Give the preparation type.
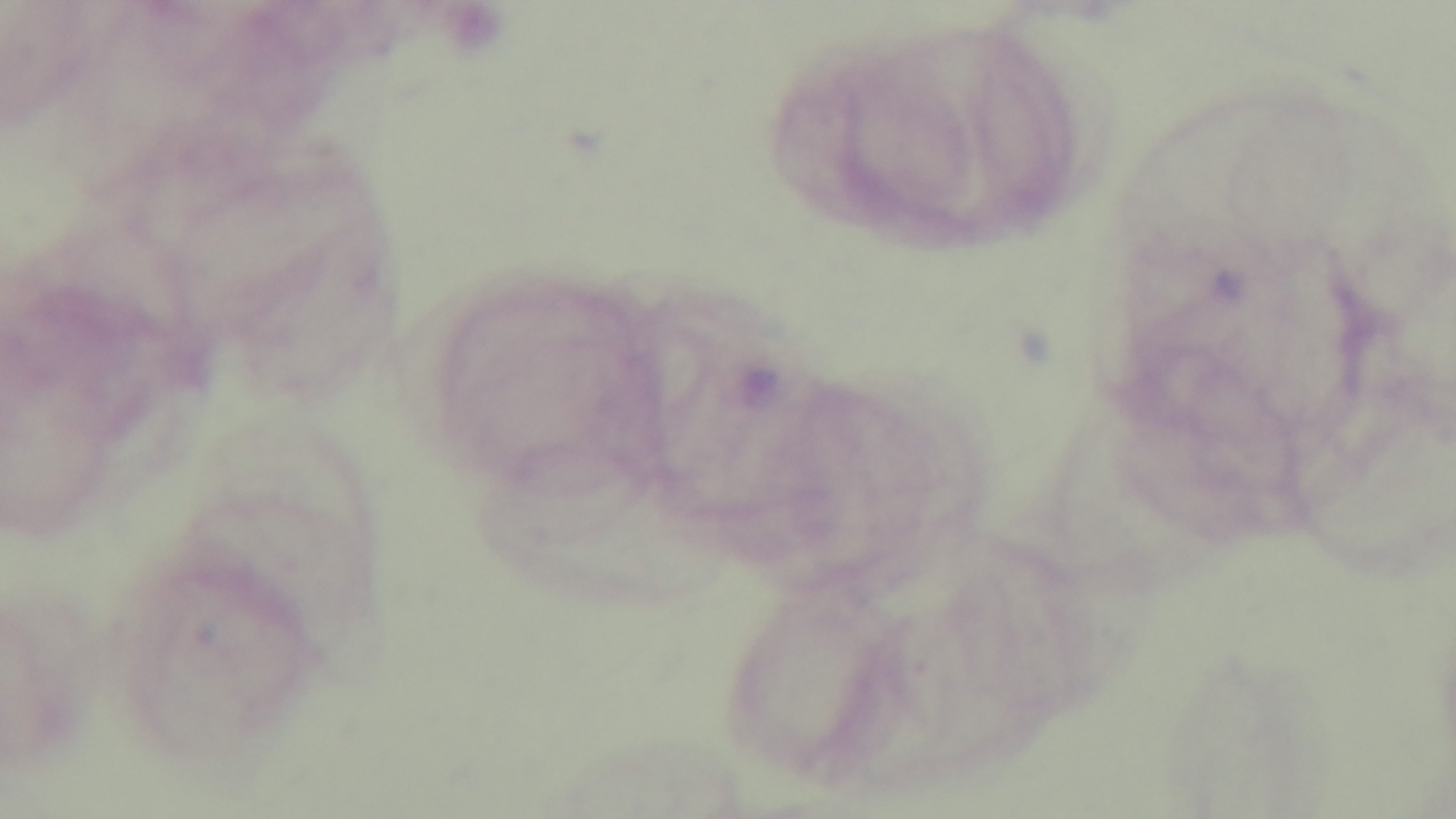
Thick.

malaria status = uninfected
objective = 100x oil immersion
capture = mounted 4K digital camera
modality = light microscopy
field of view = one from the slide
stain = Giemsa